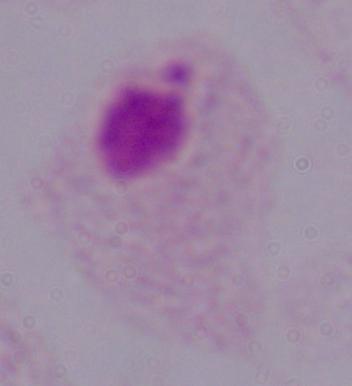
modality: photomicrograph
magnification: 1000x
identification: trichomonad